Report the malaria status of this cell.
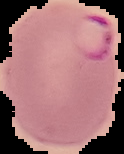
It is parasitized.

From a thin blood film. Image is 124×154 pixels. Cell region segmented out of the field of view; the surrounding area is masked to black.